Report the malaria status of this cell.
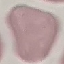

Uninfected.

Summary:
  - Image type: cell patch, automatically extracted from a larger field of view and resized to 64 × 64 pixels
  - Stain: Giemsa
  - Capture: smartphone camera at the microscope eyepiece
  - Preparation: thin blood film